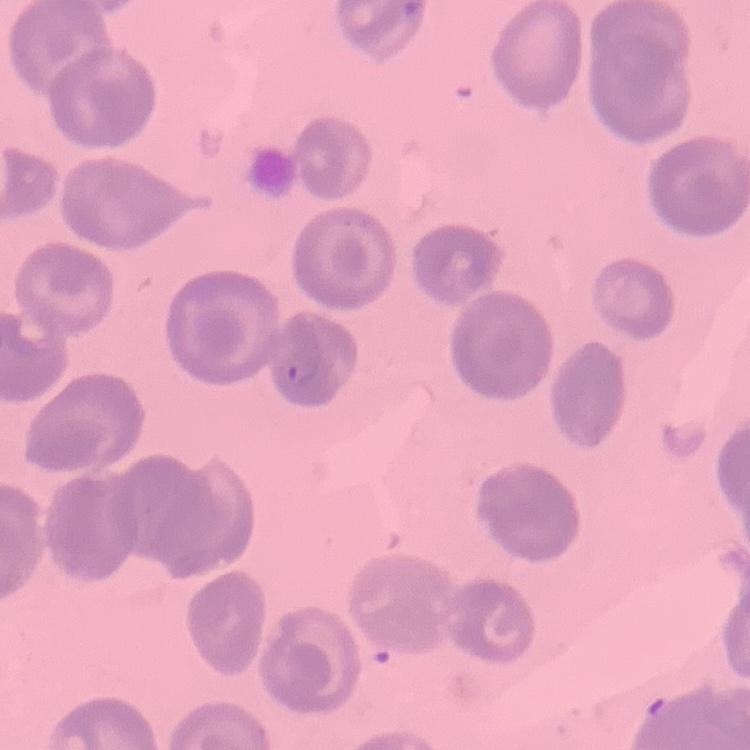

red blood cell morphology = no rouleaux formation
stain = Field's or Giemsa
image type = one tile cut from a larger photomicrograph
preparation = thin blood film